Identify the parasite.
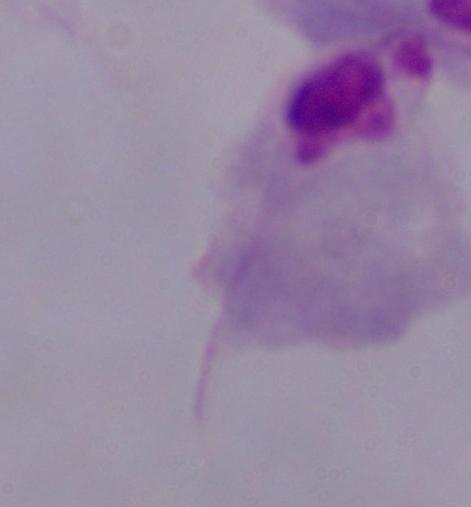
A trichomonad.

magnification = 1000x
modality = micrograph